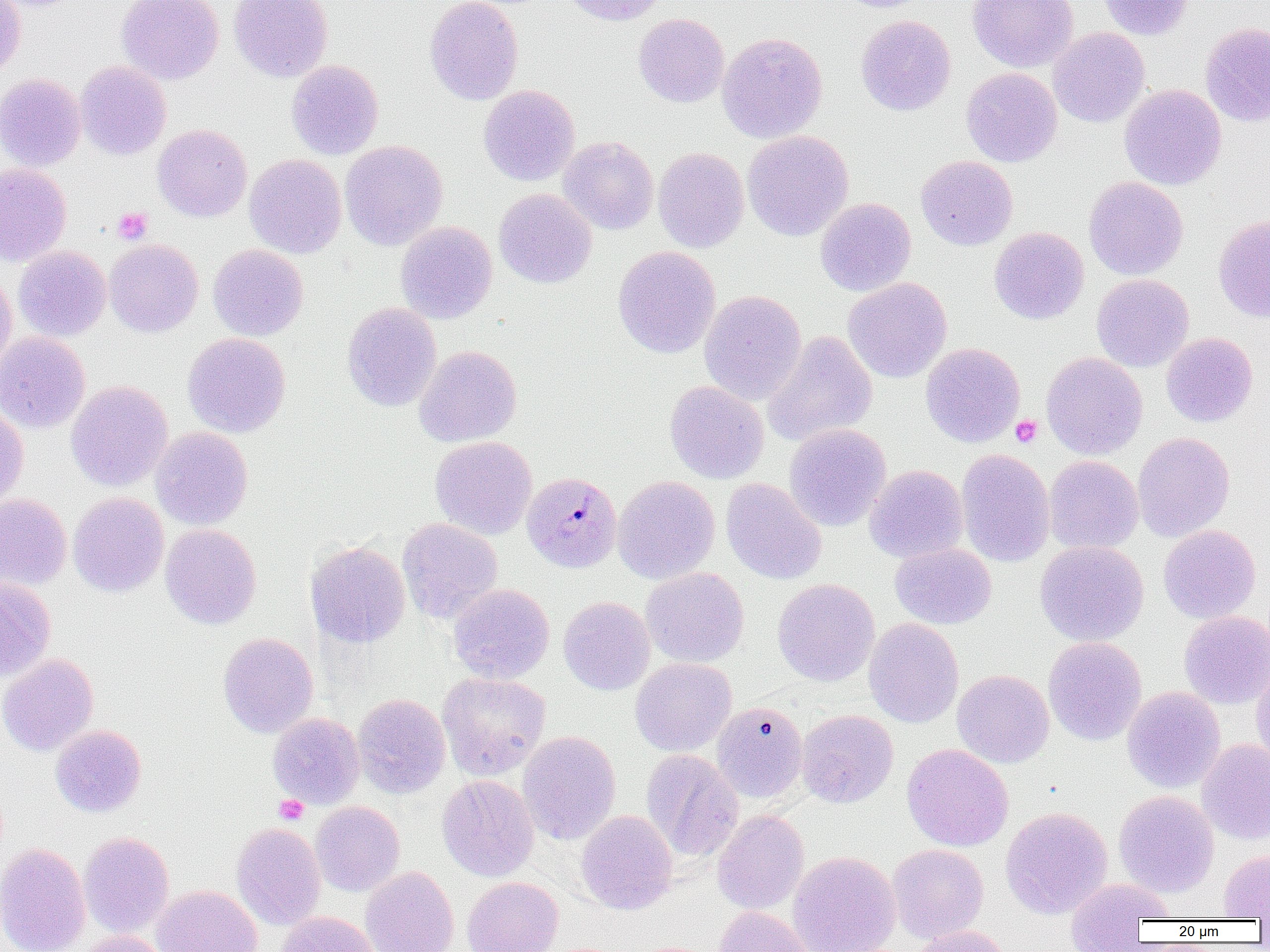
Approximate bounding boxes as (x1,y1)-(x2,y2) corner pairs in pixels. Platelet locations: (113,207)-(153,244), (1011,415)-(1042,447), (274,794)-(309,824). Uninfected red blood cell locations: (0,0)-(25,80), (116,0)-(224,84), (229,0)-(333,82), (424,0)-(523,105), (562,0)-(666,27), (834,0)-(934,13), (967,0)-(1079,72), (1097,0)-(1193,40), (633,13)-(729,108), (855,15)-(956,116), (1200,23)-(1270,126), (1048,27)-(1149,128), (717,31)-(828,143), (286,60)-(384,159), (76,61)-(171,160), (961,67)-(1062,167), (0,73)-(86,171), (479,84)-(580,186), (1119,84)-(1226,190), (153,124)-(252,222), (742,130)-(854,242), (558,136)-(659,234), (340,140)-(448,250), (653,147)-(749,252), (244,154)-(346,258), (916,155)-(1017,250), (0,163)-(72,266), (1083,176)-(1188,280), (494,188)-(596,289), (815,197)-(916,296), (1213,214)-(1270,322), (395,221)-(497,323), (989,226)-(1088,324), (104,239)-(203,337), (208,244)-(308,341), (13,246)-(111,341), (613,246)-(721,358), (0,269)-(17,375), (1091,274)-(1194,372), (843,277)-(952,383), (699,289)-(807,405), (342,302)-(441,411), (762,331)-(878,446), (0,332)-(90,434), (182,332)-(291,438), (1161,332)-(1258,427), (920,342)-(1024,447), (414,345)-(522,447), (1041,352)-(1147,460), (66,380)-(173,491), (664,381)-(769,484), (0,402)-(28,508), (784,424)-(891,531), (150,427)-(253,530), (1133,432)-(1235,542), (429,436)-(537,540), (956,449)-(1055,567), (1044,455)-(1143,554), (865,465)-(968,563), (613,475)-(720,584), (721,478)-(827,584), (68,492)-(169,598), (0,494)-(72,591), (397,518)-(503,624), (160,524)-(261,629), (1158,524)-(1261,623), (1035,540)-(1149,646), (305,541)-(410,647), (890,543)-(996,629), (641,567)-(749,667), (0,576)-(56,681), (772,579)-(880,687), (448,583)-(554,683), (558,596)-(655,695), (1179,610)-(1270,709), (863,618)-(964,728), (217,632)-(318,738), (1043,636)-(1146,745), (0,653)-(99,756), (630,658)-(736,756), (1252,659)-(1270,770), (952,669)-(1054,768), (437,672)-(550,780), (1122,686)-(1225,793), (353,694)-(450,798), (712,701)-(808,803), (796,710)-(898,808), (267,712)-(364,809), (50,725)-(146,817), (517,731)-(620,845), (1196,739)-(1270,845), (902,743)-(1014,851), (641,749)-(743,862), (437,775)-(539,881), (1114,790)-(1219,897), (310,802)-(405,896), (1000,806)-(1113,918), (712,809)-(809,915), (576,810)-(677,915), (231,823)-(326,930), (78,832)-(174,937), (0,842)-(90,952), (886,843)-(989,943), (1219,849)-(1270,919), (787,851)-(900,952), (360,866)-(459,952), (462,876)-(563,952), (1064,877)-(1175,947), (151,885)-(263,952), (713,906)-(816,952), (278,912)-(379,952), (908,925)-(1014,952), (71,931)-(170,952). Plasmodium malariae-infected red blood cell locations: (522,470)-(622,572). Slide-level diagnosis: Plasmodium malariae. Image is 1270×952 pixels. Single field of view. Thin blood film. Captured at 1000x magnification. Light microscopy.